Describe the morphology of the red blood cells.
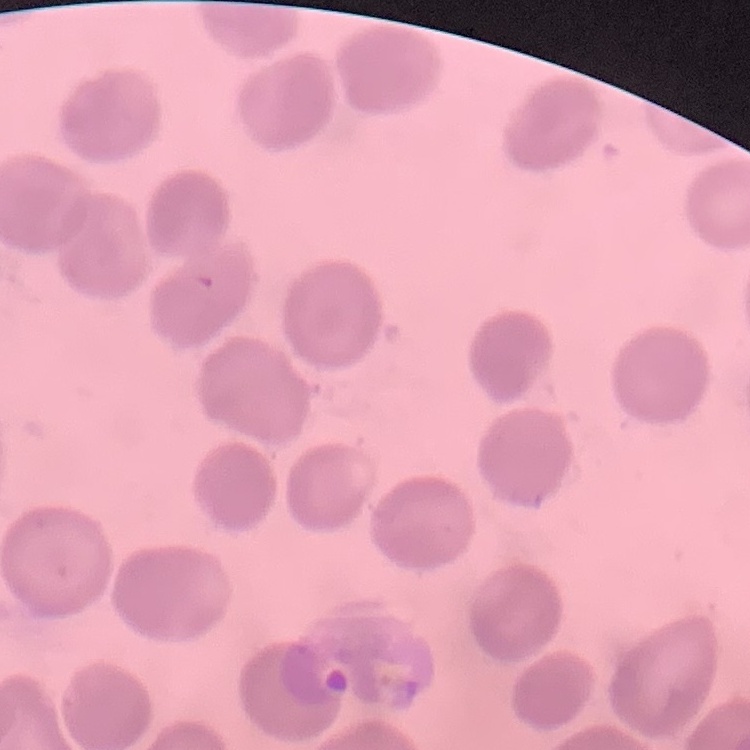

They show no rouleaux formation.

Stained with either Field's or Giemsa. Thin blood smear. Square crop of a larger photomicrograph.